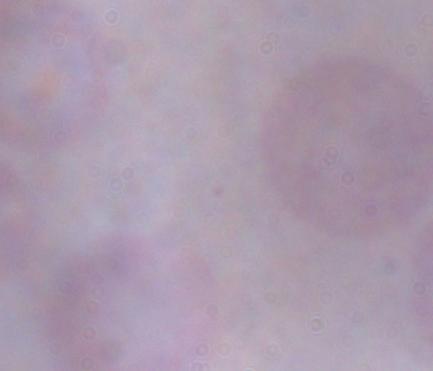
{
  "modality": "photomicrograph",
  "identification": "trypanosome",
  "magnification": "1000x"
}